Identify the parasite.
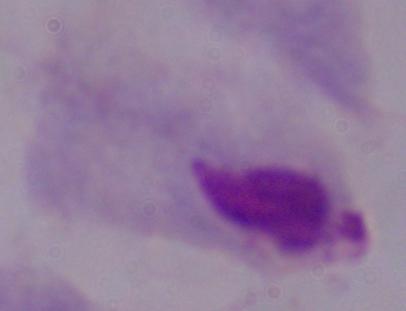
This is a trichomonad.

magnification: 1000x
modality: photomicrograph